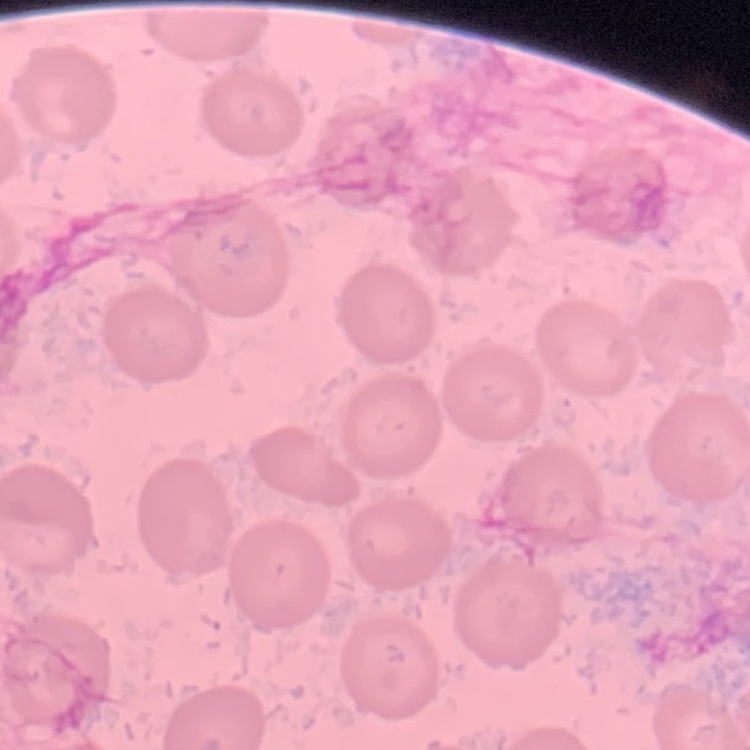

Summary:
  - Red blood cell morphology: no rouleaux formation
  - Preparation: thin blood film
  - Image type: square crop of a larger photomicrograph
  - Stain: Field's or Giemsa